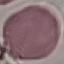

Summary:
  - Malaria status: uninfected
  - Stain: Giemsa
  - Image type: cell patch, automatically extracted from a larger field of view and resized to 64 × 64 pixels
  - Capture: smartphone camera at the microscope eyepiece
  - Preparation: thin blood smear